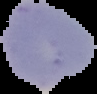
{
  "image_size": "97×94 pixels",
  "result": "no Plasmodium parasites seen",
  "preparation": "thin blood smear",
  "image_type": "cell region segmented out of the field of view; surrounding area masked to black"
}